Locate every blood parasite and identify its species.
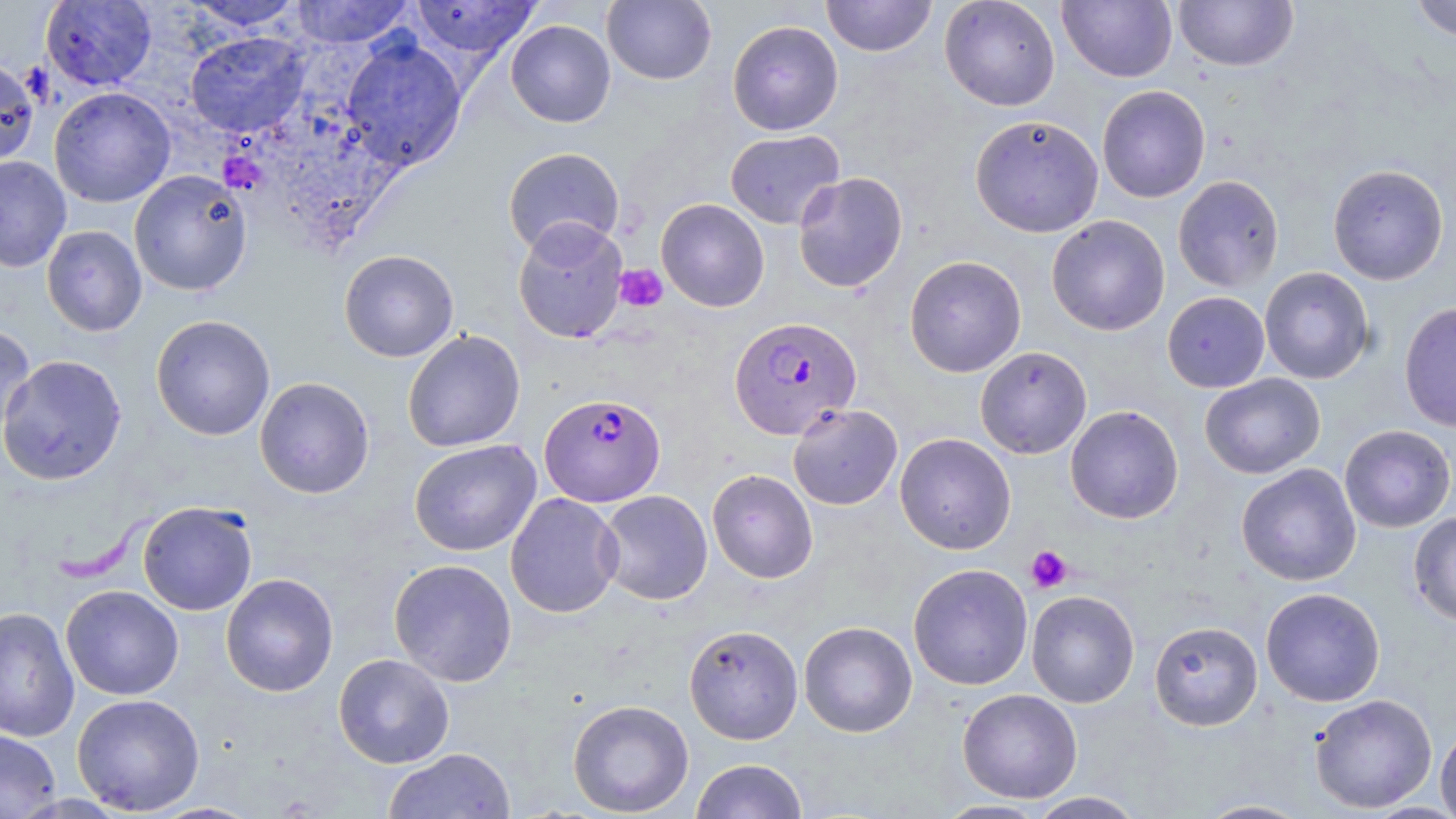
Approximate bounding boxes as named x1/y1/x2/y2 corners in pixels.
Plasmodium falciparum-infected red blood cells: (x1=729, y1=316, x2=862, y2=439), (x1=539, y1=393, x2=665, y2=507).
No Plasmodium ovale, Plasmodium malariae, Plasmodium vivax, Babesia divergens, or Trypanosoma brucei observed.

Summary:
  - Platelet locations: (x1=614, y1=264, x2=668, y2=312), (x1=1025, y1=545, x2=1073, y2=593)
  - Uninfected red blood cell locations: (x1=40, y1=0, x2=157, y2=91), (x1=409, y1=0, x2=541, y2=62), (x1=602, y1=0, x2=717, y2=85), (x1=821, y1=0, x2=937, y2=57), (x1=939, y1=0, x2=1060, y2=111), (x1=1057, y1=0, x2=1177, y2=82), (x1=1173, y1=0, x2=1299, y2=72), (x1=1409, y1=0, x2=1456, y2=42), (x1=178, y1=1, x2=308, y2=32), (x1=288, y1=1, x2=415, y2=48), (x1=505, y1=20, x2=616, y2=128), (x1=727, y1=20, x2=844, y2=135), (x1=185, y1=31, x2=310, y2=137), (x1=340, y1=37, x2=467, y2=171), (x1=0, y1=58, x2=40, y2=167), (x1=1096, y1=85, x2=1211, y2=203), (x1=49, y1=87, x2=175, y2=208), (x1=970, y1=114, x2=1104, y2=237), (x1=725, y1=129, x2=845, y2=229), (x1=503, y1=147, x2=625, y2=256), (x1=0, y1=156, x2=71, y2=272), (x1=1327, y1=163, x2=1449, y2=285), (x1=129, y1=169, x2=252, y2=296), (x1=792, y1=172, x2=908, y2=293), (x1=1172, y1=175, x2=1284, y2=293), (x1=656, y1=198, x2=770, y2=312), (x1=1046, y1=214, x2=1170, y2=336), (x1=512, y1=218, x2=629, y2=345), (x1=42, y1=225, x2=147, y2=337), (x1=339, y1=249, x2=459, y2=362), (x1=904, y1=255, x2=1027, y2=377), (x1=1259, y1=266, x2=1374, y2=384), (x1=1162, y1=291, x2=1269, y2=393), (x1=1398, y1=301, x2=1456, y2=433), (x1=150, y1=314, x2=275, y2=441), (x1=0, y1=321, x2=36, y2=442), (x1=402, y1=329, x2=525, y2=453), (x1=975, y1=346, x2=1092, y2=459), (x1=0, y1=354, x2=127, y2=486), (x1=1200, y1=373, x2=1326, y2=479), (x1=254, y1=376, x2=375, y2=499), (x1=787, y1=403, x2=903, y2=510), (x1=1065, y1=405, x2=1184, y2=524), (x1=1339, y1=424, x2=1455, y2=532), (x1=895, y1=433, x2=1016, y2=555), (x1=408, y1=439, x2=541, y2=556), (x1=1236, y1=463, x2=1362, y2=586), (x1=707, y1=469, x2=818, y2=583), (x1=597, y1=490, x2=713, y2=605), (x1=505, y1=492, x2=623, y2=618), (x1=137, y1=501, x2=258, y2=616), (x1=1408, y1=511, x2=1456, y2=627), (x1=388, y1=558, x2=517, y2=687), (x1=908, y1=563, x2=1034, y2=691), (x1=221, y1=573, x2=339, y2=697), (x1=61, y1=585, x2=183, y2=700), (x1=1260, y1=587, x2=1385, y2=707), (x1=1026, y1=590, x2=1140, y2=708), (x1=0, y1=606, x2=80, y2=743), (x1=798, y1=620, x2=918, y2=738), (x1=1149, y1=620, x2=1263, y2=731), (x1=683, y1=624, x2=803, y2=744), (x1=333, y1=653, x2=455, y2=768), (x1=957, y1=688, x2=1083, y2=803), (x1=71, y1=693, x2=205, y2=815), (x1=1309, y1=694, x2=1437, y2=813), (x1=567, y1=699, x2=694, y2=816), (x1=1435, y1=724, x2=1456, y2=819), (x1=0, y1=727, x2=62, y2=819), (x1=383, y1=747, x2=516, y2=818), (x1=690, y1=758, x2=809, y2=819), (x1=1027, y1=791, x2=1146, y2=818), (x1=1194, y1=798, x2=1314, y2=818), (x1=934, y1=799, x2=1049, y2=818)
  - Slide-level diagnosis: Plasmodium falciparum
  - Magnification: 1000x
  - Image size: 1456×819 pixels
  - Stain: May-Grünwald-Giemsa
  - Preparation: thin blood film
  - Modality: light microscopy
  - Field of view: one of a larger specimen